Locate every malaria parasite and every leukocyte.
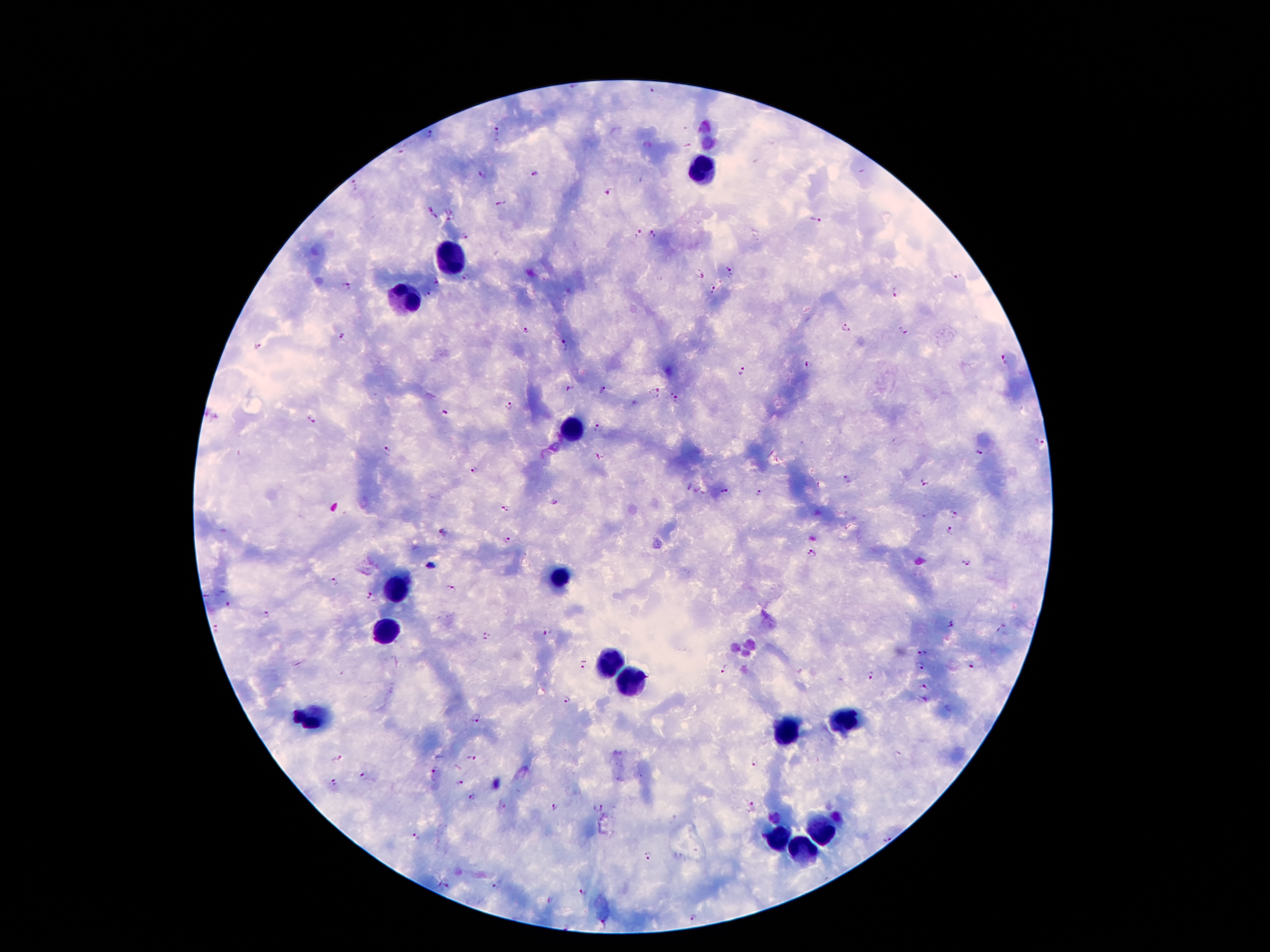
Approximate centers as {x, y} in pixels.
Malaria parasites: {574, 88}, {652, 91}, {497, 130}, {431, 133}, {400, 153}, {534, 173}, {483, 174}, {607, 192}, {501, 205}, {427, 207}, {450, 214}, {436, 217}, {817, 222}, {639, 233}, {653, 233}, {464, 236}, {730, 272}, {700, 275}, {954, 275}, {468, 279}, {437, 283}, {347, 286}, {714, 291}, {428, 293}, {897, 294}, {846, 330}, {526, 332}, {902, 332}, {342, 336}, {563, 344}, {257, 346}, {1004, 359}, {810, 365}, {741, 371}, {569, 388}, {604, 391}, {654, 392}, {674, 397}, {510, 408}, {447, 415}, {310, 419}, {598, 427}, {1040, 442}, {387, 451}, {980, 452}, {597, 456}, {472, 471}, {847, 478}, {925, 482}, {687, 486}, {725, 491}, {760, 493}, {554, 502}, {505, 508}, {955, 513}, {948, 531}, {445, 532}, {508, 540}, {812, 552}, {965, 564}, {430, 565}, {333, 582}, {450, 588}, {369, 596}, {229, 604}, {267, 615}, {949, 623}, {217, 629}, {546, 631}, {485, 635}, {924, 653}, {584, 664}, {921, 666}, {724, 667}, {973, 668}, {870, 675}, {925, 687}, {566, 700}, {476, 717}, {339, 757}, {469, 758}, {757, 763}, {432, 772}, {363, 779}, {333, 784}, {461, 784}, {472, 798}, {502, 805}, {597, 806}, {554, 807}, {749, 807}, {774, 818}, {415, 835}, {886, 838}, {648, 856}, {445, 884}, {497, 884}, {580, 893}, {552, 902}, {694, 919}, {604, 924}.
Leukocytes: {704, 170}, {450, 262}, {405, 301}, {571, 435}, {561, 576}, {400, 588}, {383, 632}, {606, 660}, {620, 679}, {314, 721}, {845, 724}, {791, 731}, {821, 828}, {776, 840}, {801, 852}.

field of view = single
patient malaria status = infected with Plasmodium falciparum
preparation = thick blood film
capture = smartphone camera through the microscope eyepiece
magnification = 100x
image size = 1270×952 pixels
stain = Giemsa